Report the malaria status of this cell.
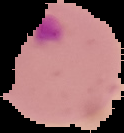
It is parasitized.

The area outside the segmented cell region is set to black. From a thin blood film. Image is 124×133 pixels.